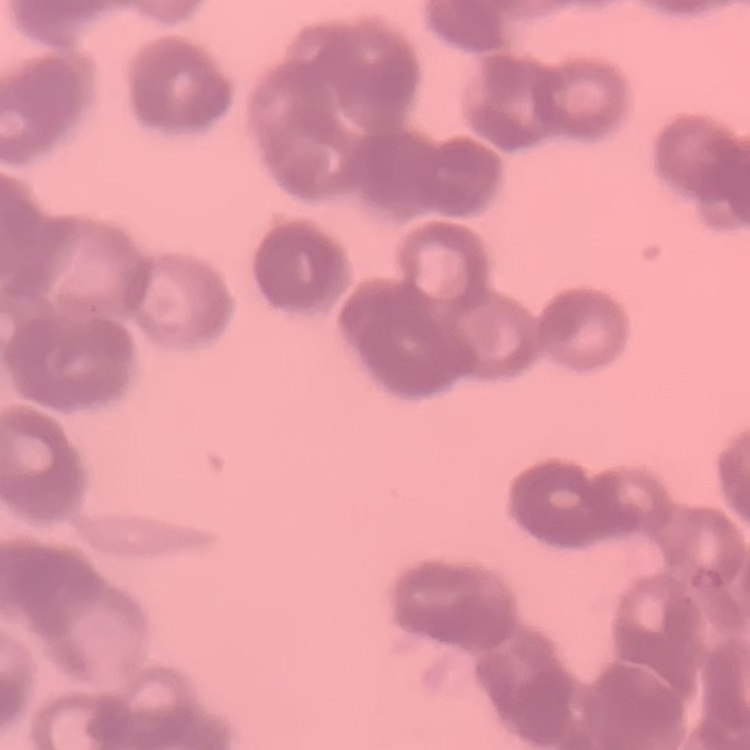

The erythrocytes show rouleaux formation. Field's or Giemsa stain. Square crop of a larger photomicrograph. Thin peripheral smear.